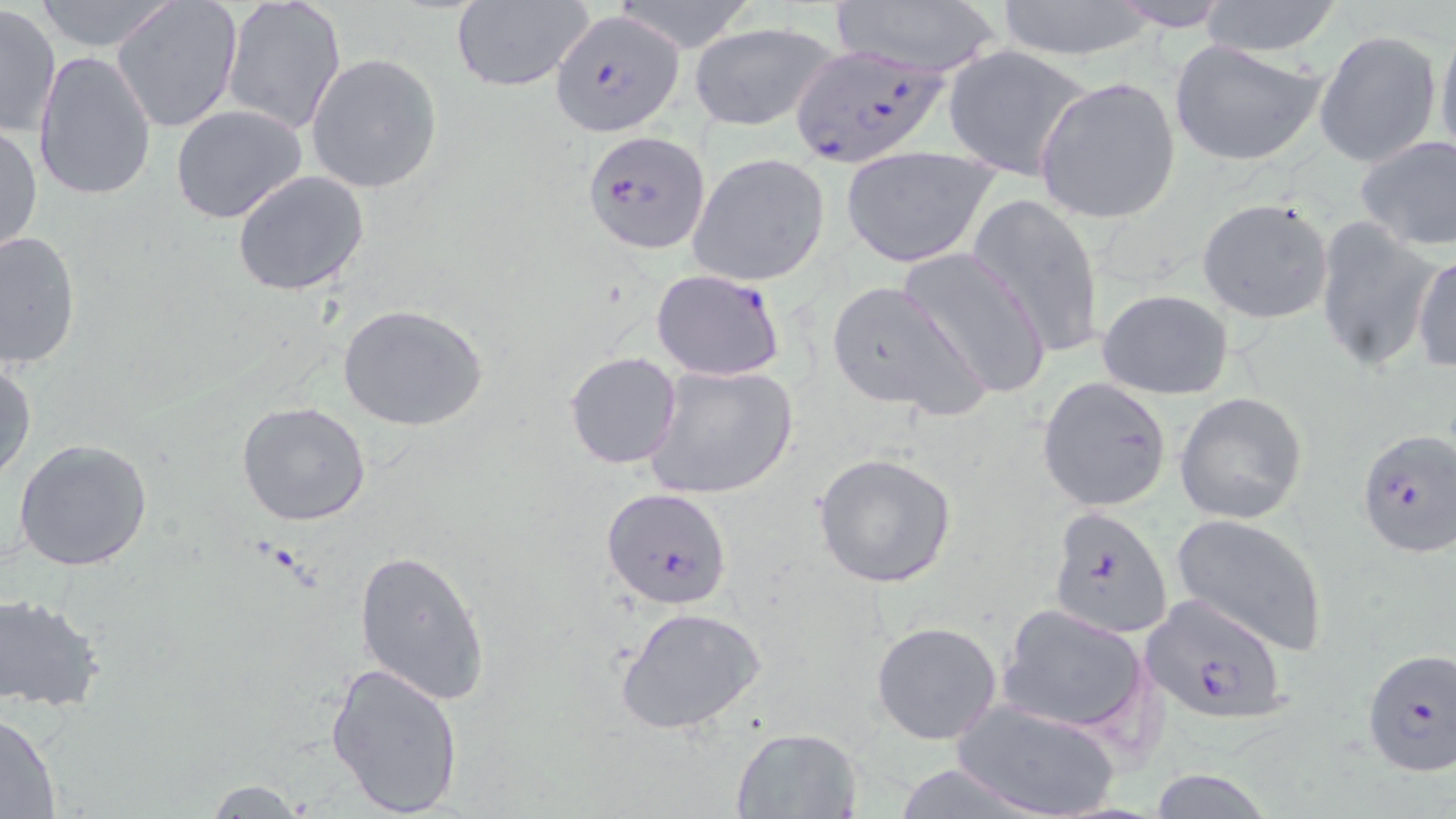 Approximate bounding boxes as (x1,y1)-(x2,y2) corner pairs in pixels. Plasmodium falciparum-infected red blood cell locations: (550,8)-(685,137), (789,42)-(951,169), (582,130)-(712,255), (650,268)-(788,383), (1354,428)-(1456,558), (601,488)-(733,611), (1047,505)-(1172,638), (1141,594)-(1288,723), (1361,649)-(1454,777). Uninfected red blood cell locations: (111,0)-(242,134), (220,0)-(348,136), (607,0)-(759,53), (826,0)-(1011,75), (1105,0)-(1235,32), (30,1)-(181,52), (447,1)-(596,92), (992,1)-(1158,61), (1195,1)-(1344,58), (0,4)-(60,140), (688,20)-(841,132), (1437,25)-(1456,161), (1314,31)-(1442,171), (1169,39)-(1327,167), (941,44)-(1093,181), (33,49)-(158,202), (305,53)-(443,194), (1034,76)-(1181,225), (172,104)-(309,224), (1,122)-(42,259), (1355,135)-(1456,253), (840,145)-(998,268), (687,152)-(831,288), (231,169)-(370,297), (968,194)-(1105,359), (1196,196)-(1335,323), (1313,217)-(1442,373), (0,229)-(80,370), (897,247)-(1051,401), (1412,250)-(1456,375), (826,278)-(986,418), (1097,289)-(1235,400), (339,304)-(487,431), (564,350)-(683,469), (1,361)-(37,482), (644,362)-(798,501), (1037,376)-(1173,512), (1175,392)-(1308,524), (237,401)-(371,526), (13,439)-(155,574), (812,453)-(958,590), (1170,513)-(1329,657), (354,548)-(490,704), (0,593)-(105,711), (999,603)-(1151,737), (613,604)-(770,738), (871,620)-(1003,745), (323,663)-(465,817), (954,699)-(1124,819), (0,709)-(62,816), (729,727)-(863,818), (888,762)-(1047,819), (1145,768)-(1278,819), (199,779)-(312,817). Slide-level diagnosis: Plasmodium falciparum. Thin blood film. May-Grünwald-Giemsa stain. Image is 1456×819 pixels. Single field of view. Light microscopy. Captured at 1000x magnification.